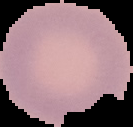

preparation = thin blood film
result = no malaria parasites seen
image size = 133×127 pixels
image type = cell region segmented out of the field of view; surrounding area masked to black